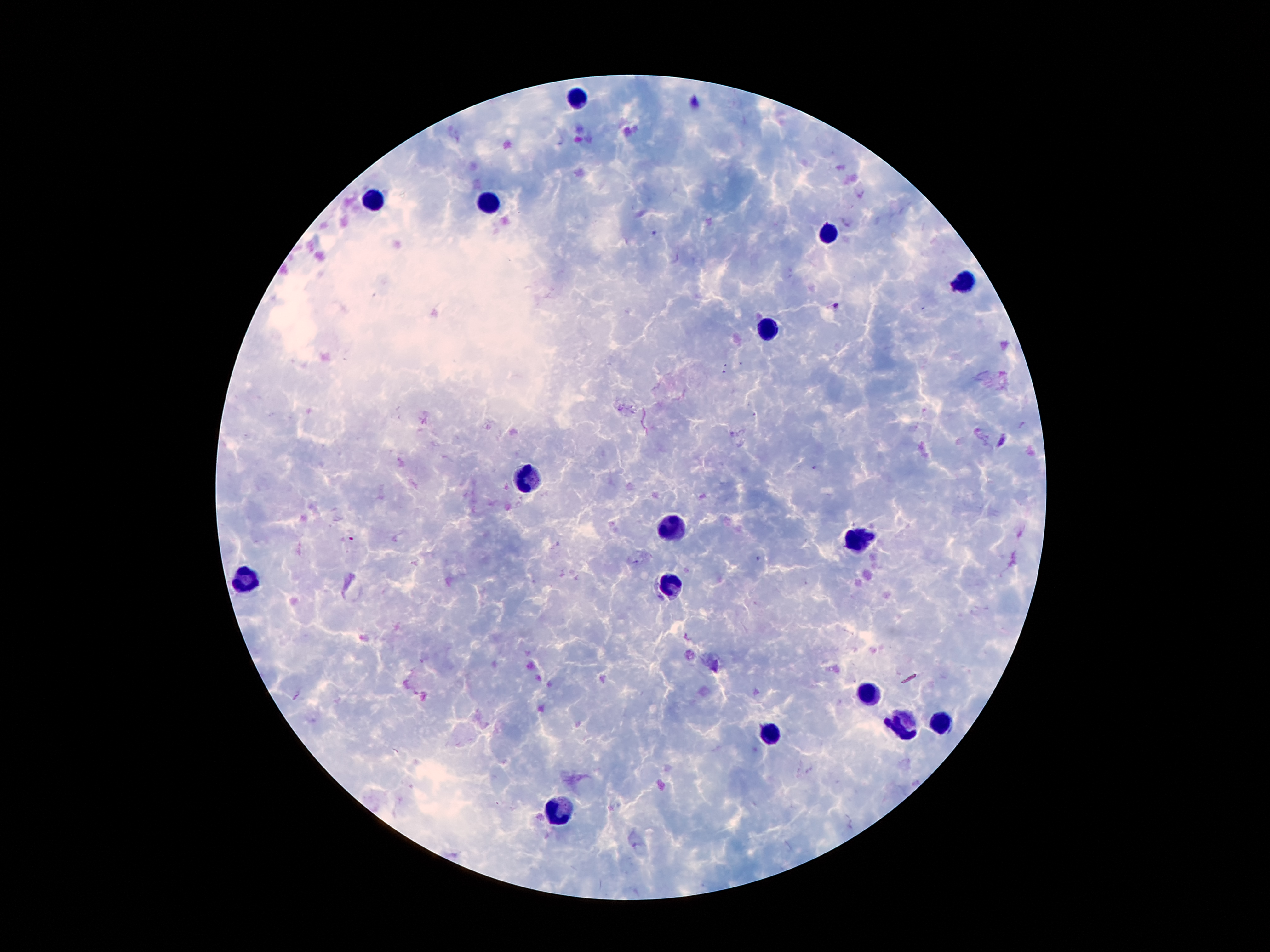
{
  "plasmodium_parasite_locations": "approximate centers as {x, y} in pixels: {837, 306}",
  "preparation": "thick peripheral-blood smear",
  "leukocyte_locations": "approximate centers as {x, y} in pixels: {580, 99}, {374, 200}, {492, 203}, {828, 232}, {966, 282}, {770, 329}, {531, 479}, {675, 527}, {859, 540}, {252, 580}, {669, 585}, {868, 695}, {942, 722}, {903, 723}, {770, 736}, {562, 811}",
  "image_size": "1270×952 pixels",
  "patient_malaria_status": "positive for Plasmodium falciparum",
  "magnification": "100x",
  "capture": "smartphone through the microscope eyepiece",
  "field_of_view": "single",
  "stain": "Giemsa"
}